Assess for malaria.
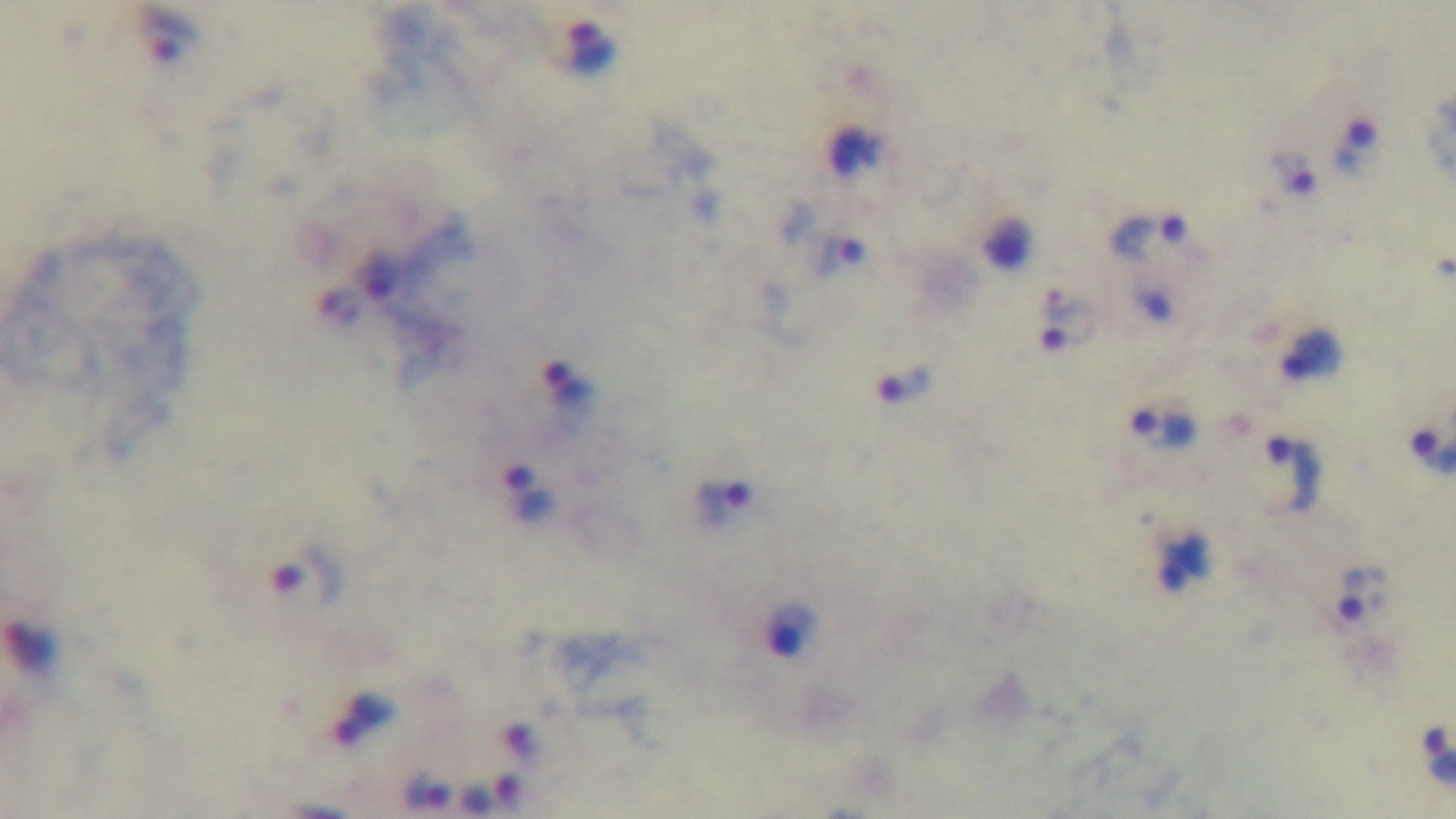

Infected.

Summary:
  - Objective: 100x oil immersion
  - Stain: Giemsa
  - Preparation: thick
  - Capture: mounted 4K digital camera
  - Modality: light microscopy
  - Field of view: one from the slide